State which parasite is depicted.
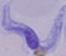
This is a trypanosome.

Summary:
  - Modality: photomicrograph
  - Magnification: 1000x